Identify the parasite.
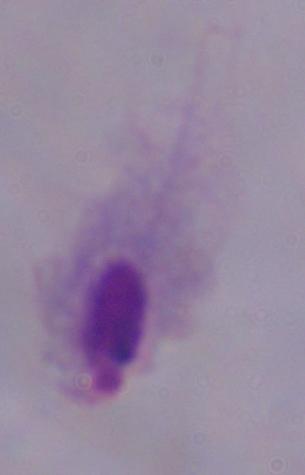
A trichomonad.

modality = photomicrograph
magnification = 1000x